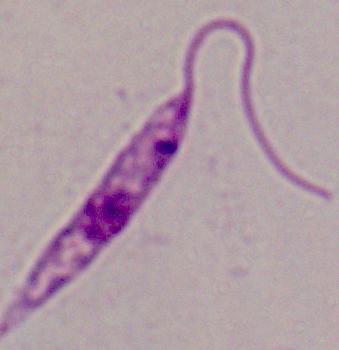
{
  "magnification": "1000x",
  "modality": "micrograph",
  "identification": "Leishmania"
}